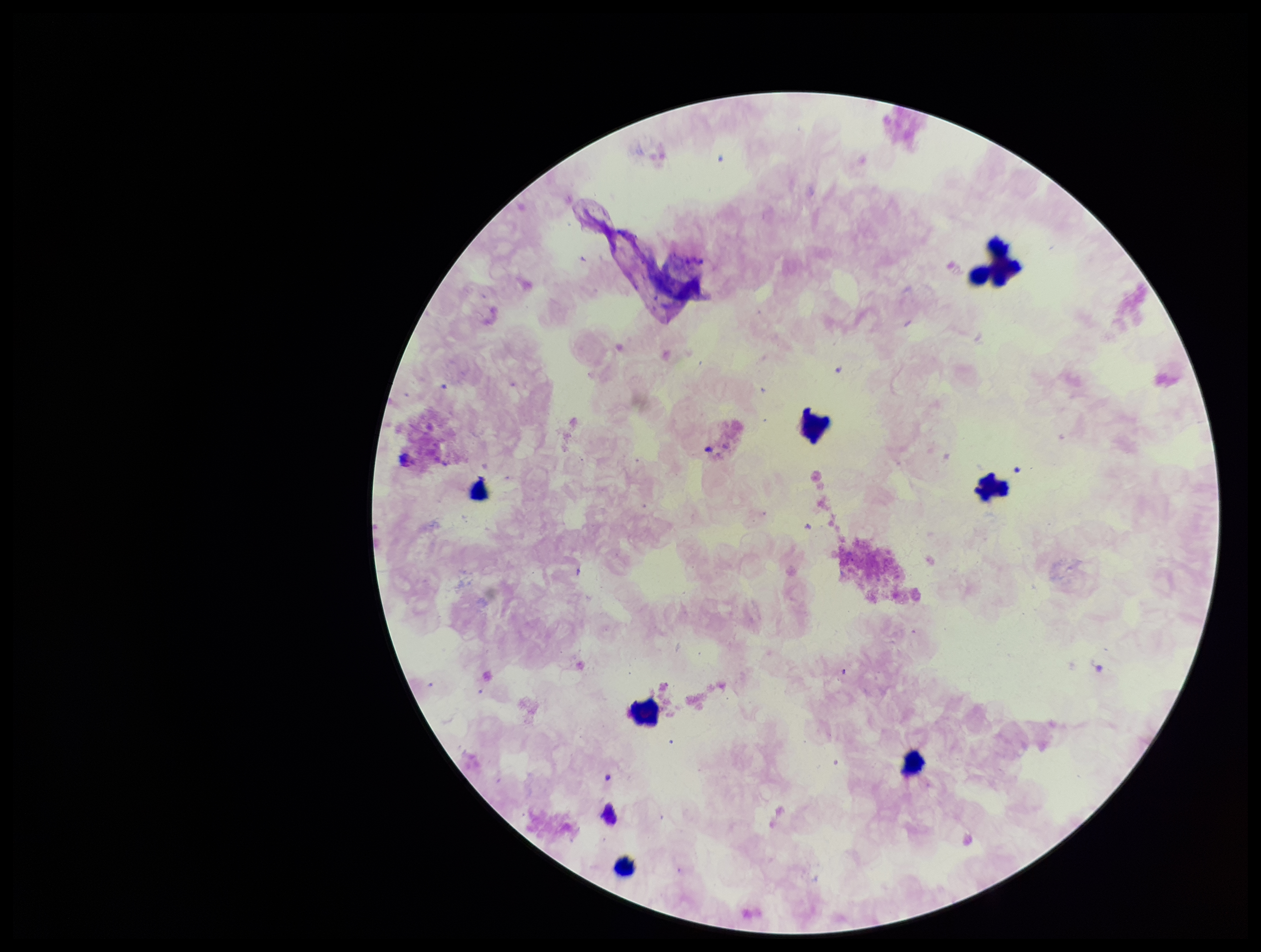
{
  "field_of_view": "single",
  "leukocyte_count": 6,
  "parasite_count": 0,
  "image_size": "1261×952 pixels",
  "patient_malaria_status": "negative",
  "stain": "Giemsa",
  "preparation": "thick",
  "capture": "smartphone photograph through the microscope eyepiece",
  "plasmodium_parasites": "none seen"
}